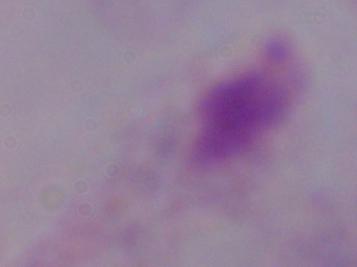

Summary:
  - Magnification: 1000x
  - Modality: photomicrograph
  - Identification: trichomonad